Outline each Plasmodium falciparum-infected red blood cell.
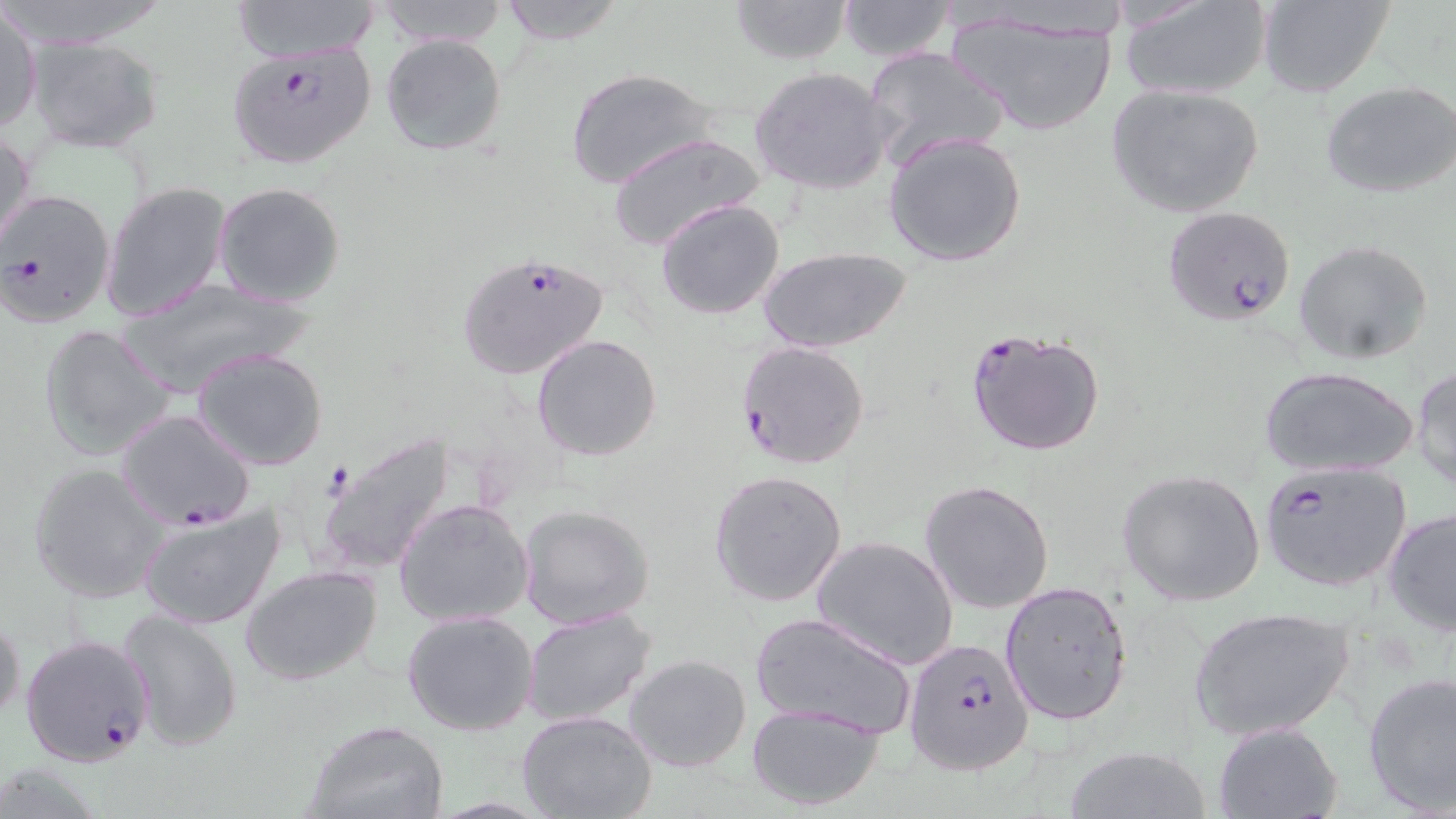
Approximate bounding boxes as [x1, y1, x2, y2] in pixels.
Plasmodium falciparum-infected red blood cells: [228, 41, 374, 171], [0, 187, 117, 327], [1163, 208, 1297, 326], [456, 254, 610, 381], [965, 327, 1107, 457], [735, 339, 870, 470], [116, 409, 254, 530], [1259, 461, 1410, 592], [19, 634, 154, 768], [903, 637, 1035, 775].

Summary:
  - Uninfected red blood cell locations: [231, 0, 381, 63], [374, 0, 510, 48], [497, 0, 626, 44], [729, 0, 855, 64], [834, 0, 958, 61], [1118, 0, 1271, 102], [1259, 1, 1395, 99], [946, 8, 1122, 137], [1, 10, 42, 137], [380, 33, 508, 158], [26, 35, 166, 154], [862, 46, 1009, 170], [565, 67, 722, 190], [749, 67, 895, 196], [1322, 81, 1456, 200], [1105, 83, 1265, 218], [1, 127, 36, 256], [882, 129, 1028, 268], [608, 132, 764, 253], [214, 182, 346, 305], [102, 183, 233, 323], [655, 198, 786, 320], [1294, 239, 1434, 365], [758, 245, 914, 351], [111, 279, 316, 400], [39, 323, 178, 462], [532, 334, 662, 461], [192, 347, 330, 471], [1258, 365, 1418, 478], [1410, 365, 1456, 491], [318, 434, 455, 577], [29, 464, 167, 604], [708, 469, 848, 607], [1116, 469, 1265, 609], [920, 479, 1055, 615], [394, 498, 535, 628], [139, 502, 285, 630], [517, 504, 655, 631], [1382, 506, 1456, 634], [810, 535, 959, 671], [240, 565, 383, 685], [1000, 580, 1133, 725], [1187, 605, 1357, 743], [117, 608, 244, 753], [521, 608, 660, 728], [402, 611, 538, 736], [750, 612, 918, 739], [0, 613, 23, 727], [624, 654, 752, 772], [1361, 672, 1456, 815], [745, 703, 885, 811], [516, 709, 657, 819], [302, 720, 450, 819], [1213, 721, 1343, 818], [1063, 744, 1210, 819]
  - Slide-level diagnosis: Plasmodium falciparum
  - Stain: May-Grünwald-Giemsa
  - Field of view: single
  - Image size: 1456×819 pixels
  - Preparation: thin blood film
  - Modality: optical microscopy
  - Magnification: 1000x